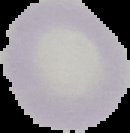

Summary:
  - Preparation: thin blood smear
  - Result: no malaria parasites seen
  - Image size: 130×133 pixels
  - Image type: segmented cell region with the area outside set to black